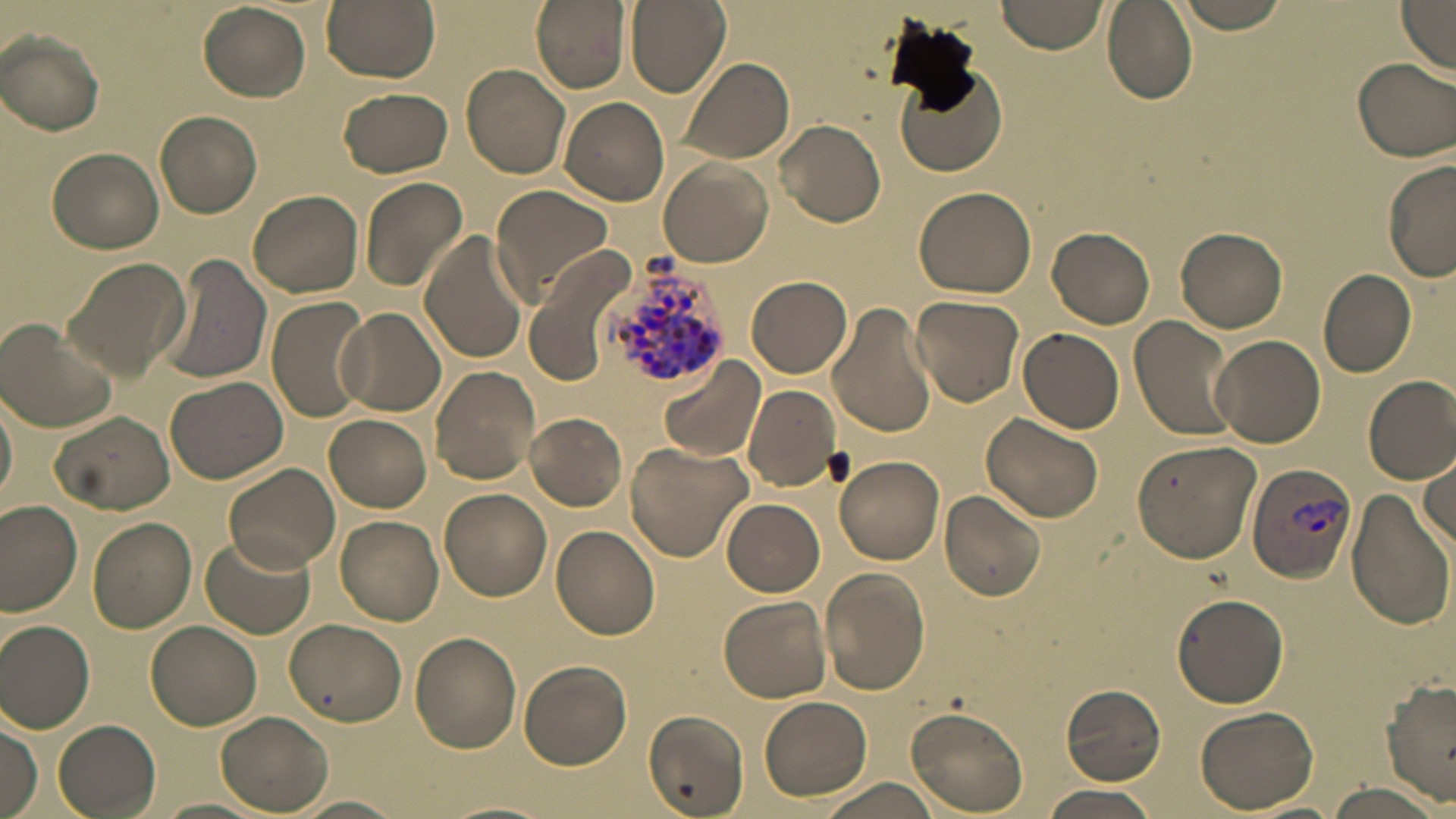
slide-level diagnosis = Plasmodium vivax
image size = 1456×819 pixels
uninfected red blood cell locations = approximate bounding boxes as named x1/y1/x2/y2 corners in pixels: (x1=321, y1=0, x2=439, y2=81), (x1=530, y1=0, x2=629, y2=93), (x1=626, y1=0, x2=730, y2=96), (x1=996, y1=0, x2=1104, y2=54), (x1=1172, y1=0, x2=1293, y2=33), (x1=198, y1=2, x2=311, y2=102), (x1=1104, y1=3, x2=1196, y2=104), (x1=1395, y1=3, x2=1455, y2=73), (x1=2, y1=30, x2=105, y2=135), (x1=1352, y1=55, x2=1455, y2=163), (x1=677, y1=57, x2=795, y2=165), (x1=895, y1=60, x2=1009, y2=178), (x1=462, y1=64, x2=572, y2=181), (x1=339, y1=87, x2=454, y2=178), (x1=559, y1=97, x2=670, y2=205), (x1=156, y1=110, x2=263, y2=218), (x1=777, y1=120, x2=886, y2=228), (x1=48, y1=147, x2=165, y2=254), (x1=1382, y1=158, x2=1456, y2=283), (x1=659, y1=159, x2=772, y2=267), (x1=358, y1=176, x2=468, y2=294), (x1=914, y1=184, x2=1038, y2=297), (x1=490, y1=185, x2=614, y2=303), (x1=248, y1=189, x2=363, y2=297), (x1=1048, y1=227, x2=1156, y2=327), (x1=1175, y1=227, x2=1287, y2=332), (x1=418, y1=230, x2=532, y2=366), (x1=156, y1=253, x2=273, y2=386), (x1=520, y1=254, x2=631, y2=389), (x1=64, y1=256, x2=188, y2=380), (x1=1319, y1=268, x2=1417, y2=378), (x1=747, y1=275, x2=850, y2=377), (x1=910, y1=294, x2=1025, y2=405), (x1=266, y1=298, x2=371, y2=422), (x1=828, y1=300, x2=939, y2=437), (x1=338, y1=308, x2=445, y2=415), (x1=1129, y1=316, x2=1238, y2=444), (x1=1, y1=318, x2=118, y2=435), (x1=1018, y1=326, x2=1124, y2=434), (x1=1210, y1=333, x2=1326, y2=447), (x1=660, y1=359, x2=763, y2=464), (x1=430, y1=366, x2=540, y2=484), (x1=1363, y1=375, x2=1455, y2=484), (x1=165, y1=376, x2=291, y2=485), (x1=744, y1=384, x2=842, y2=490), (x1=0, y1=394, x2=16, y2=510), (x1=51, y1=410, x2=175, y2=514), (x1=525, y1=412, x2=627, y2=510), (x1=984, y1=412, x2=1106, y2=525), (x1=324, y1=415, x2=431, y2=511), (x1=1131, y1=439, x2=1262, y2=564), (x1=626, y1=443, x2=751, y2=559), (x1=1417, y1=454, x2=1454, y2=549), (x1=834, y1=455, x2=944, y2=565), (x1=225, y1=461, x2=340, y2=574), (x1=441, y1=488, x2=552, y2=600), (x1=939, y1=489, x2=1045, y2=599), (x1=1347, y1=489, x2=1452, y2=629), (x1=722, y1=498, x2=824, y2=596), (x1=0, y1=502, x2=83, y2=616), (x1=335, y1=517, x2=442, y2=625), (x1=88, y1=518, x2=197, y2=631), (x1=552, y1=525, x2=661, y2=639), (x1=199, y1=531, x2=314, y2=640), (x1=822, y1=568, x2=931, y2=695), (x1=1172, y1=593, x2=1289, y2=708), (x1=719, y1=596, x2=831, y2=703), (x1=0, y1=619, x2=95, y2=732), (x1=285, y1=619, x2=406, y2=727), (x1=148, y1=620, x2=261, y2=729), (x1=410, y1=631, x2=522, y2=752), (x1=518, y1=659, x2=631, y2=769), (x1=1382, y1=680, x2=1456, y2=805), (x1=1060, y1=686, x2=1167, y2=785), (x1=758, y1=696, x2=871, y2=801), (x1=906, y1=706, x2=1030, y2=815), (x1=1196, y1=706, x2=1318, y2=812), (x1=215, y1=709, x2=333, y2=813), (x1=644, y1=710, x2=749, y2=817), (x1=52, y1=718, x2=161, y2=818), (x1=1, y1=721, x2=41, y2=819), (x1=820, y1=778, x2=946, y2=819), (x1=1322, y1=782, x2=1446, y2=817), (x1=1039, y1=786, x2=1163, y2=819), (x1=294, y1=794, x2=406, y2=818), (x1=156, y1=797, x2=267, y2=817)
Plasmodium vivax-infected red blood cell locations = approximate bounding boxes as named x1/y1/x2/y2 corners in pixels: (x1=594, y1=255, x2=733, y2=395), (x1=1248, y1=464, x2=1358, y2=583)
preparation = thin blood film
stain = May-Grünwald-Giemsa
modality = light microscopy
magnification = 1000x
field of view = single